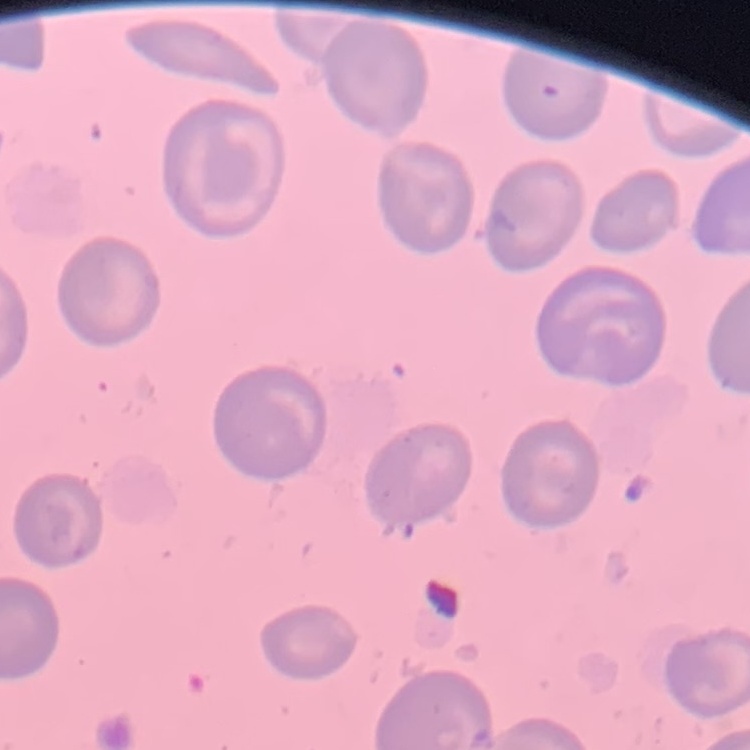
The erythrocytes exhibit no rouleaux formation. Field's or Giemsa stain. Thin peripheral smear. One tile cut from a larger photomicrograph.